Outline each blood parasite and name the species.
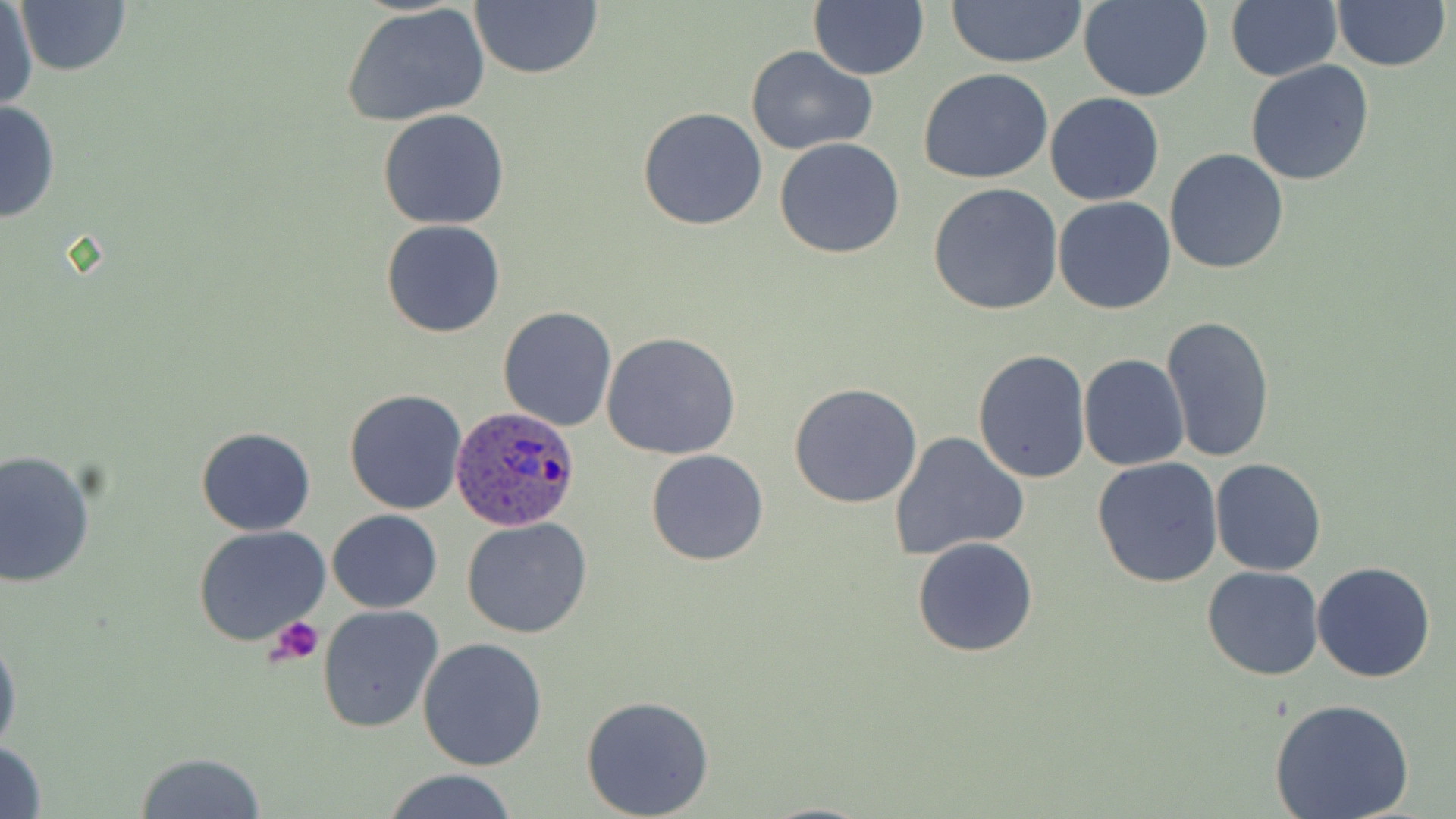
Approximate bounding boxes as [x1, y1, x2, y2] in pixels.
Plasmodium ovale-infected red blood cells: [452, 405, 582, 530].
No Plasmodium falciparum, Plasmodium malariae, Plasmodium vivax, Babesia divergens, or Trypanosoma brucei observed.

{
  "slide_level_diagnosis": "Plasmodium ovale",
  "stain": "May-Grünwald-Giemsa",
  "preparation": "thin blood film",
  "platelet_locations": "approximate bounding boxes as [x1, y1, x2, y2] in pixels: [268, 615, 325, 665]",
  "modality": "light microscopy",
  "magnification": "1000x",
  "field_of_view": "single",
  "image_size": "1456×819 pixels",
  "uninfected_red_blood_cell_locations": "approximate bounding boxes as [x1, y1, x2, y2] in pixels: [468, 0, 604, 81], [807, 0, 929, 81], [943, 0, 1090, 68], [1227, 0, 1341, 81], [14, 1, 133, 76], [1080, 1, 1214, 102], [1331, 1, 1450, 73], [1, 3, 37, 112], [341, 4, 491, 127], [746, 47, 877, 156], [1244, 60, 1375, 187], [918, 68, 1055, 183], [1046, 92, 1164, 205], [0, 99, 61, 225], [638, 107, 768, 230], [378, 109, 511, 228], [774, 137, 906, 258], [1165, 149, 1290, 274], [928, 184, 1064, 316], [1053, 195, 1178, 314], [381, 220, 507, 337], [497, 305, 617, 431], [1161, 315, 1276, 463], [602, 332, 741, 462], [972, 349, 1091, 485], [1079, 355, 1190, 472], [788, 383, 922, 508], [344, 388, 469, 514], [195, 426, 315, 536], [888, 430, 1028, 560], [646, 449, 768, 566], [0, 450, 97, 588], [1210, 457, 1327, 576], [1091, 458, 1223, 589], [327, 510, 442, 613], [463, 518, 594, 639], [192, 523, 330, 646], [913, 537, 1039, 657], [1313, 561, 1436, 684], [1203, 565, 1324, 681], [317, 604, 444, 733], [0, 626, 21, 761], [416, 637, 549, 772], [579, 696, 715, 818], [1267, 698, 1416, 819], [0, 739, 48, 818], [135, 750, 268, 819], [377, 770, 520, 819]"
}